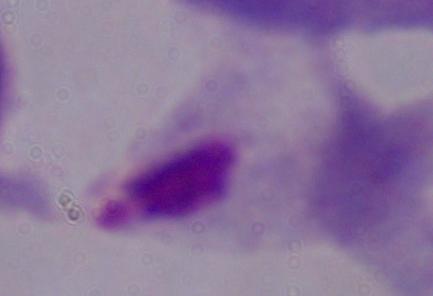

A trichomonad is shown. Captured at 1000x magnification. Micrograph.